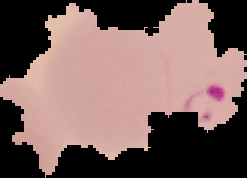

preparation = thin blood film
image type = segmented cell region with the area outside set to black
image size = 247×178 pixels
result = Plasmodium parasites identified